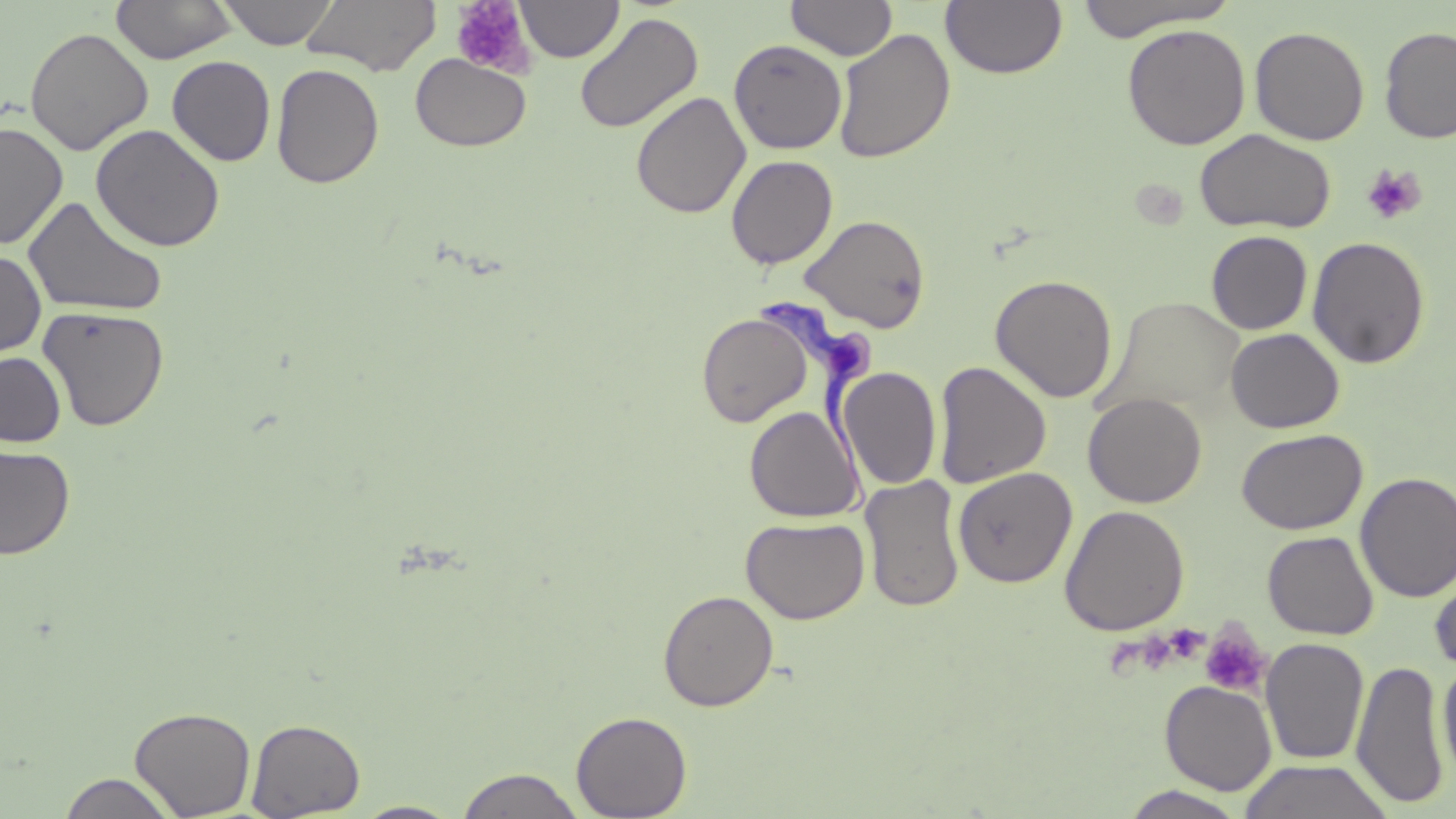
Approximate bounding boxes as named x1/y1/x2/y2 corners in pixels. Platelet locations: (x1=451, y1=1, x2=534, y2=76), (x1=1361, y1=164, x2=1427, y2=225), (x1=1199, y1=624, x2=1271, y2=697). Uninfected red blood cell locations: (x1=217, y1=0, x2=338, y2=49), (x1=302, y1=0, x2=442, y2=75), (x1=785, y1=0, x2=897, y2=61), (x1=1070, y1=0, x2=1235, y2=40), (x1=110, y1=1, x2=237, y2=64), (x1=516, y1=1, x2=623, y2=62), (x1=940, y1=1, x2=1067, y2=80), (x1=574, y1=12, x2=703, y2=135), (x1=1122, y1=23, x2=1251, y2=150), (x1=25, y1=26, x2=153, y2=156), (x1=1250, y1=26, x2=1370, y2=145), (x1=1379, y1=26, x2=1456, y2=143), (x1=832, y1=28, x2=955, y2=163), (x1=729, y1=39, x2=847, y2=155), (x1=411, y1=54, x2=531, y2=151), (x1=167, y1=56, x2=276, y2=166), (x1=271, y1=63, x2=384, y2=189), (x1=631, y1=90, x2=751, y2=220), (x1=0, y1=121, x2=69, y2=250), (x1=91, y1=124, x2=226, y2=252), (x1=1194, y1=128, x2=1336, y2=234), (x1=726, y1=155, x2=838, y2=269), (x1=22, y1=195, x2=168, y2=319), (x1=800, y1=214, x2=931, y2=333), (x1=1206, y1=230, x2=1313, y2=334), (x1=1307, y1=236, x2=1430, y2=369), (x1=0, y1=249, x2=47, y2=361), (x1=989, y1=274, x2=1118, y2=403), (x1=1104, y1=295, x2=1246, y2=416), (x1=38, y1=305, x2=170, y2=432), (x1=696, y1=311, x2=812, y2=428), (x1=1226, y1=328, x2=1344, y2=433), (x1=0, y1=352, x2=66, y2=447), (x1=934, y1=360, x2=1051, y2=489), (x1=839, y1=367, x2=942, y2=490), (x1=1083, y1=392, x2=1207, y2=508), (x1=744, y1=405, x2=864, y2=523), (x1=1237, y1=427, x2=1368, y2=534), (x1=0, y1=445, x2=76, y2=559), (x1=953, y1=466, x2=1077, y2=588), (x1=1355, y1=472, x2=1456, y2=603), (x1=859, y1=474, x2=965, y2=613), (x1=1059, y1=504, x2=1190, y2=636), (x1=740, y1=516, x2=870, y2=624), (x1=1263, y1=531, x2=1379, y2=640), (x1=1430, y1=564, x2=1456, y2=675), (x1=657, y1=589, x2=779, y2=711), (x1=1260, y1=637, x2=1369, y2=765), (x1=1350, y1=658, x2=1449, y2=810), (x1=1437, y1=659, x2=1456, y2=785), (x1=1159, y1=680, x2=1277, y2=794), (x1=129, y1=705, x2=257, y2=819), (x1=571, y1=710, x2=692, y2=818), (x1=246, y1=718, x2=365, y2=818), (x1=1238, y1=759, x2=1395, y2=818), (x1=455, y1=767, x2=587, y2=818), (x1=57, y1=772, x2=180, y2=818), (x1=1117, y1=785, x2=1252, y2=819), (x1=351, y1=801, x2=464, y2=818). Trypanosoma brucei locations: (x1=757, y1=292, x2=876, y2=519). Slide-level diagnosis: Trypanosoma brucei. Image is 1456×819 pixels. May-Grünwald-Giemsa stain. One field of a larger specimen. Captured at 1000x magnification. Thin blood smear. Light microscopy.